Point out each Plasmodium parasite.
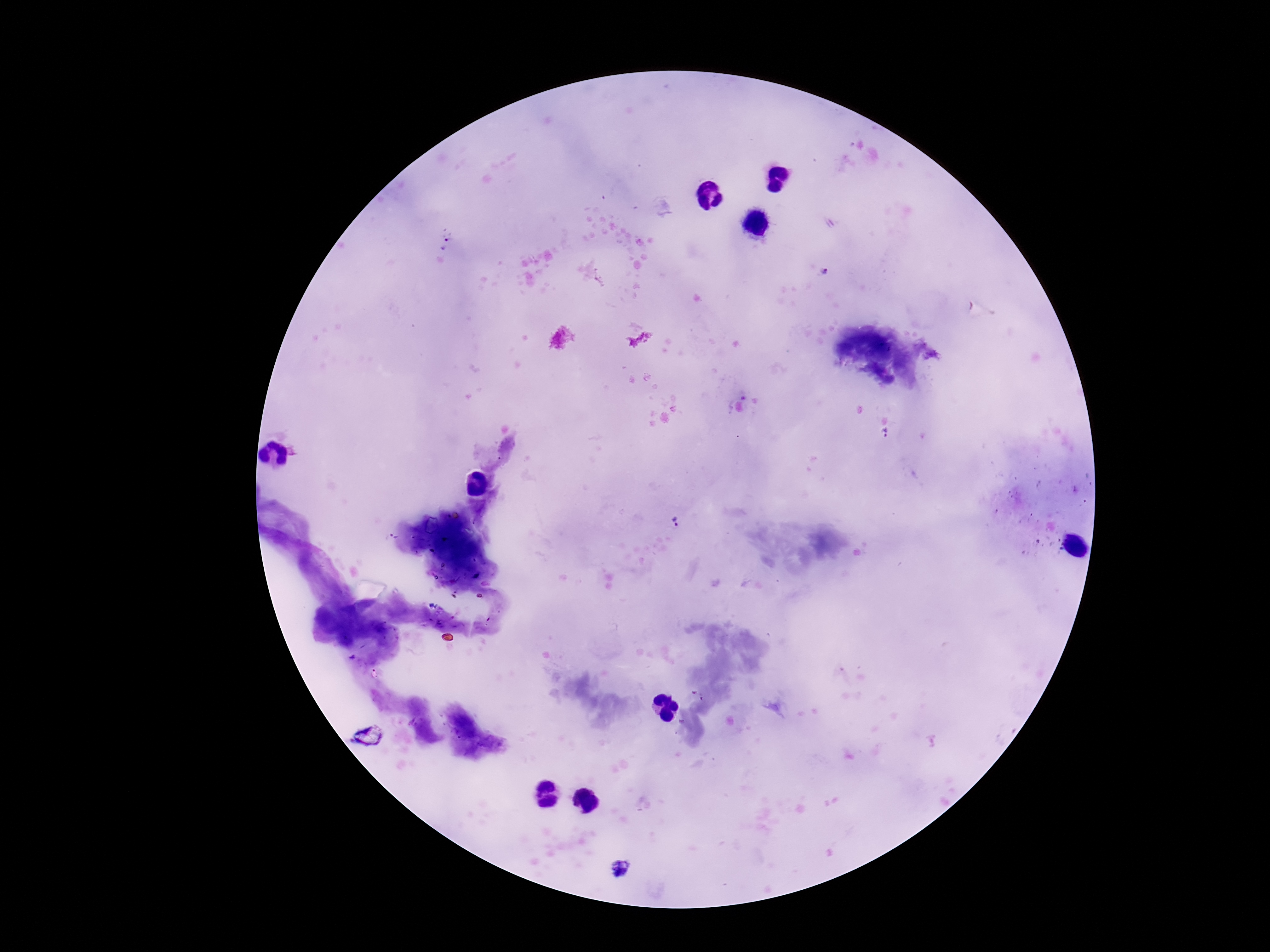

Approximate centers as {x, y} in pixels.
Plasmodium parasites: {446, 244}, {886, 433}, {677, 524}, {620, 869}.

stain = Giemsa
field of view = single
magnification = 100x
capture = smartphone camera through the microscope eyepiece
preparation = thick peripheral-blood smear
image size = 1270×952 pixels
patient malaria status = positive